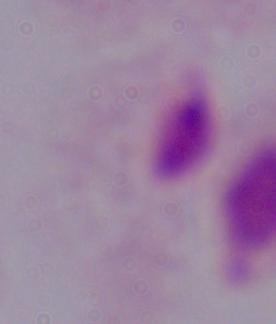
A trichomonad is seen. Micrograph. 1000x magnification.